State which cell type is depicted.
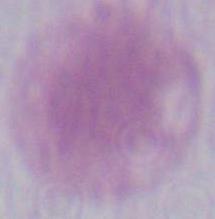

This is an erythrocyte.

modality = micrograph
magnification = 1000x